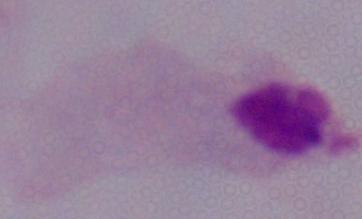
A trichomonad is seen. Micrograph. Captured at 1000x magnification.